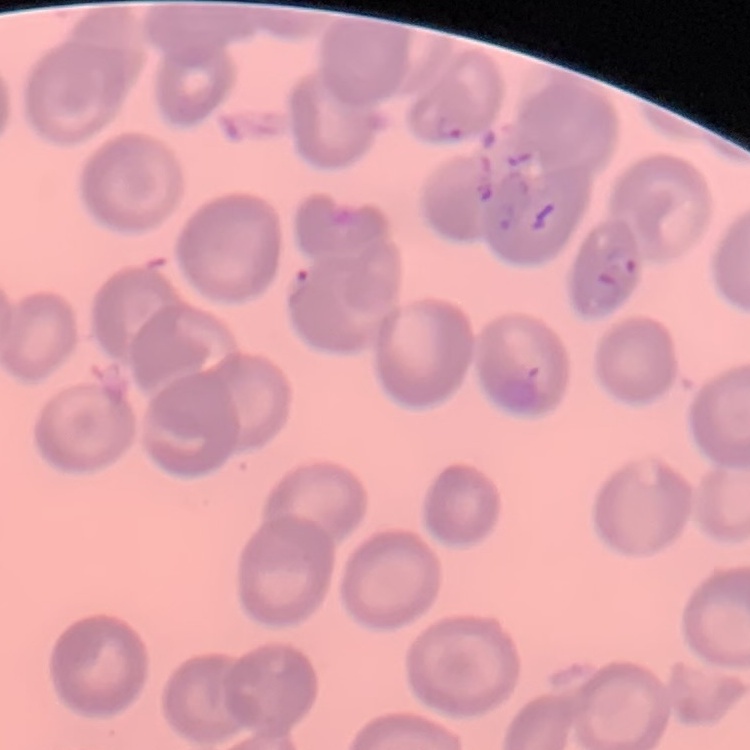
Summary:
  - Red blood cell morphology: no rouleaux formation
  - Image type: one tile cut from a larger photomicrograph
  - Stain: Field's or Giemsa
  - Preparation: thin blood film